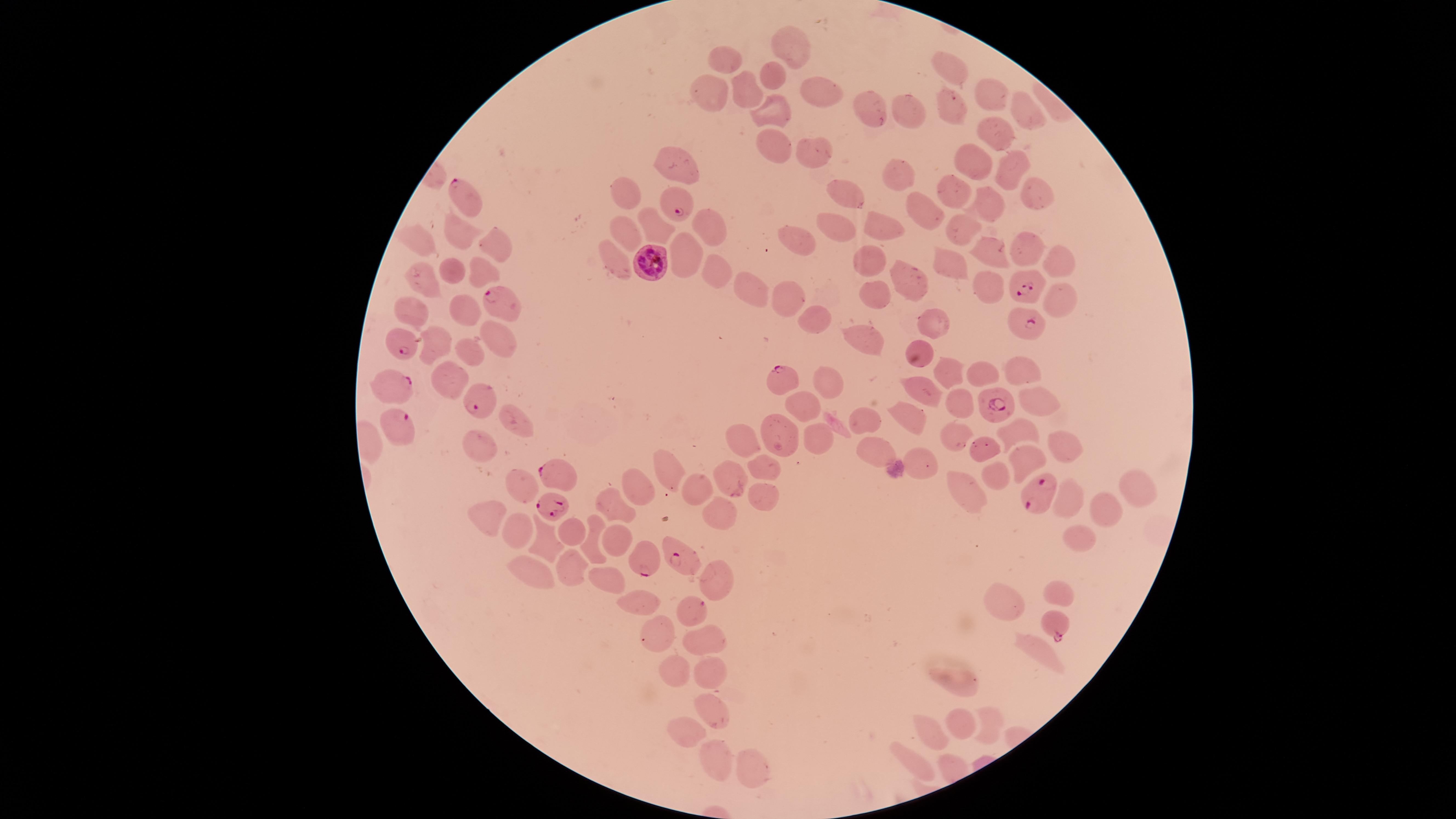

Approximate marker points as {x, y} in pixels.
Summary:
  - Parasitized RBCs: {462, 195}, {678, 201}, {648, 259}, {1030, 284}, {503, 301}, {1023, 323}, {405, 341}, {783, 377}, {387, 384}, {474, 398}, {995, 402}, {396, 429}, {556, 469}, {1040, 486}, {553, 507}, {681, 555}, {646, 560}, {690, 608}, {1057, 625}
  - Uninfected RBCs: {792, 46}, {726, 59}, {947, 71}, {773, 74}, {707, 88}, {746, 89}, {812, 89}, {987, 92}, {954, 104}, {871, 107}, {1019, 109}, {910, 111}, {770, 112}, {990, 128}, {766, 146}, {810, 152}, {973, 159}, {673, 161}, {1008, 166}, {899, 175}, {1034, 191}, {956, 192}, {623, 193}, {846, 193}, {987, 204}, {919, 210}, {703, 218}, {837, 227}, {963, 227}, {657, 230}, {883, 230}, {626, 234}, {461, 236}, {797, 236}, {418, 243}, {1019, 246}, {493, 248}, {987, 248}, {683, 253}, {611, 259}, {866, 260}, {1055, 260}, {950, 267}, {712, 270}, {450, 271}, {473, 279}, {418, 283}, {909, 285}, {987, 286}, {756, 292}, {870, 295}, {786, 300}, {1058, 303}, {412, 311}, {464, 313}, {809, 319}, {933, 323}, {499, 333}, {860, 341}, {437, 343}, {465, 348}, {921, 354}, {1018, 364}, {977, 370}, {450, 372}, {952, 373}, {825, 382}, {921, 385}, {1038, 398}, {800, 403}, {957, 409}, {864, 418}, {909, 422}, {780, 425}, {523, 426}, {1023, 429}, {743, 435}, {818, 437}, {950, 439}, {1058, 443}, {986, 448}, {873, 451}, {482, 453}, {1016, 460}, {920, 463}, {759, 469}, {671, 472}, {735, 472}, {989, 475}, {643, 480}, {697, 487}, {968, 488}, {526, 491}, {761, 494}, {1136, 494}, {1067, 498}, {614, 504}, {719, 511}, {1103, 514}, {485, 519}, {574, 529}, {518, 534}, {590, 535}, {546, 539}, {1076, 539}, {614, 544}, {567, 566}, {526, 567}, {715, 571}, {600, 576}, {1058, 592}, {1001, 598}, {645, 600}, {653, 631}, {701, 637}, {1041, 652}, {672, 663}, {707, 669}, {960, 679}, {709, 709}, {994, 715}, {965, 719}, {685, 729}, {929, 730}, {711, 760}, {913, 761}, {750, 776}
  - Image size: 1456×819 pixels
  - Species: Plasmodium falciparum
  - Capture: smartphone photograph through the microscope eyepiece
  - Presence: malaria parasites detected
  - Preparation: thin smear of blood
  - Stain: Giemsa
  - Visible region: circular
  - Field of view: single